State which cell type is depicted.
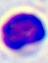

This is a leukocyte.

Photomicrograph. Captured at 400x magnification.